Report the malaria status of this cell.
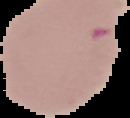
It is uninfected.

Summary:
  - Image type: segmented cell region on a black background
  - Preparation: thin blood smear
  - Image size: 130×118 pixels